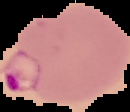
malaria_status: parasitized
image_size: 130×112 pixels
image_type: segmented cell region with the area outside set to black
preparation: thin blood film